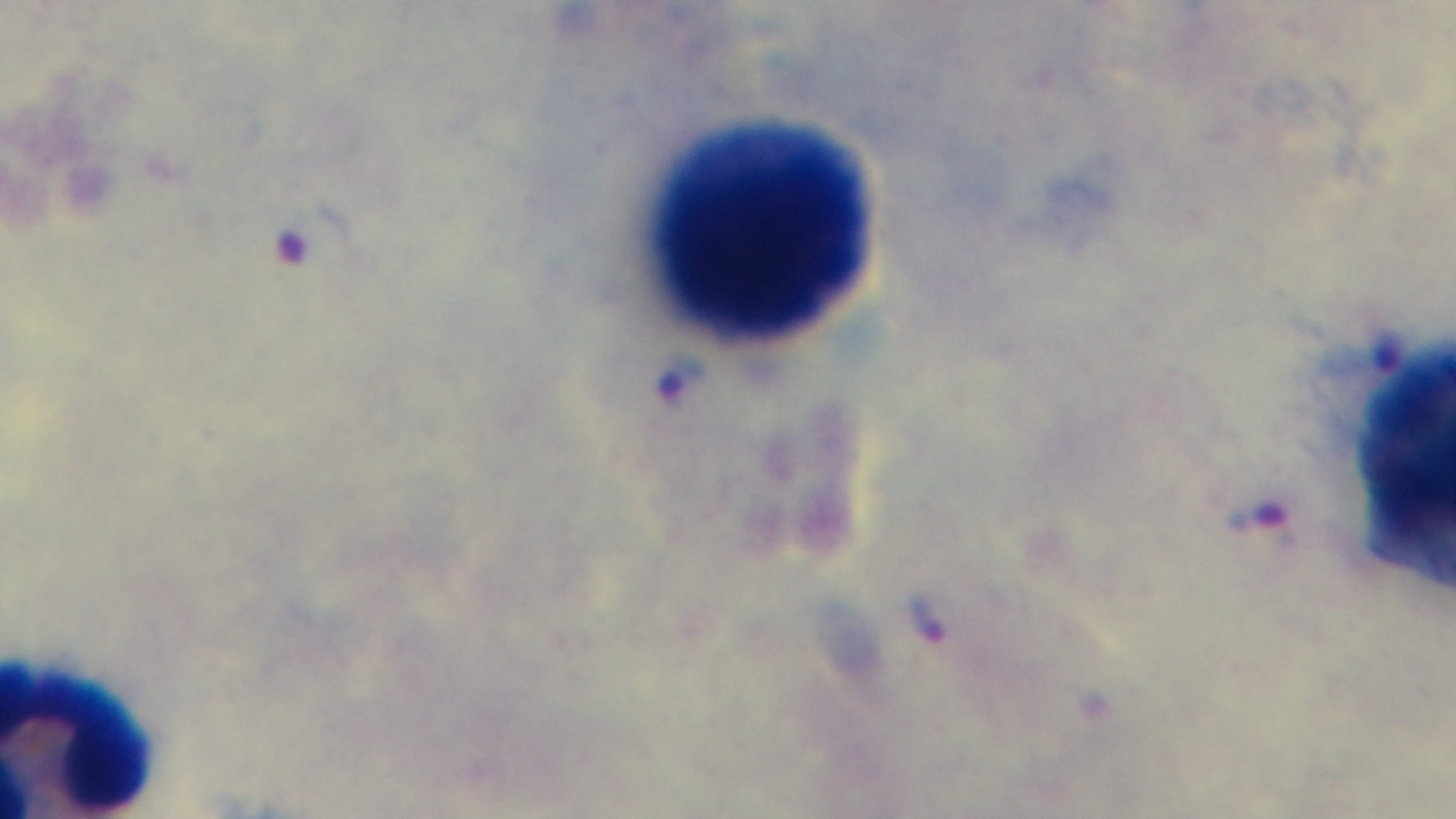

Captured with a mounted 4K digital camera. One field from the slide. Photomicrograph. Giemsa-stained. Malaria status: infected. Oil-immersion objective, 100x. Preparation: thick blood film.